Comment on the morphology of the erythrocytes.
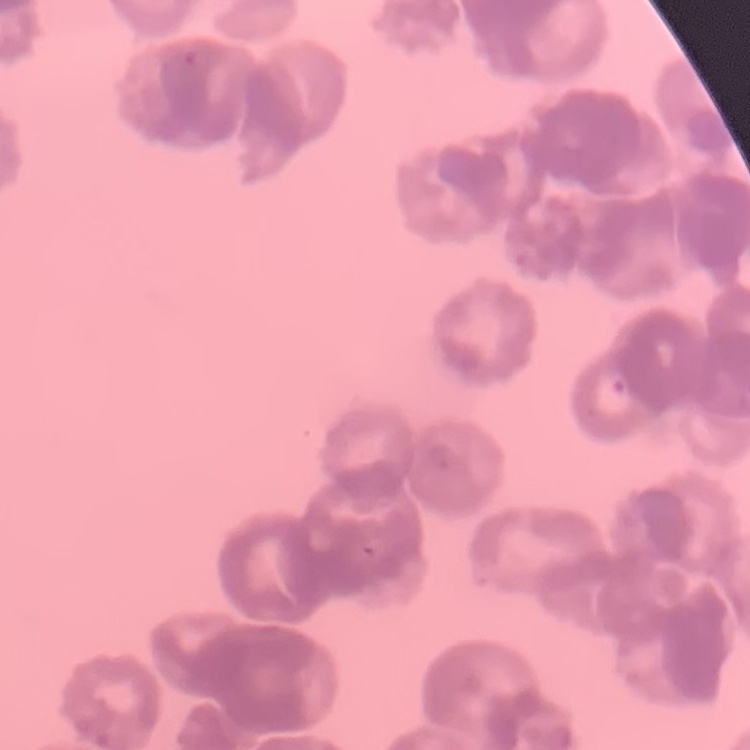
They show rouleaux formation.

One tile cut from a larger photomicrograph. Thin peripheral smear. Field's or Giemsa stain.